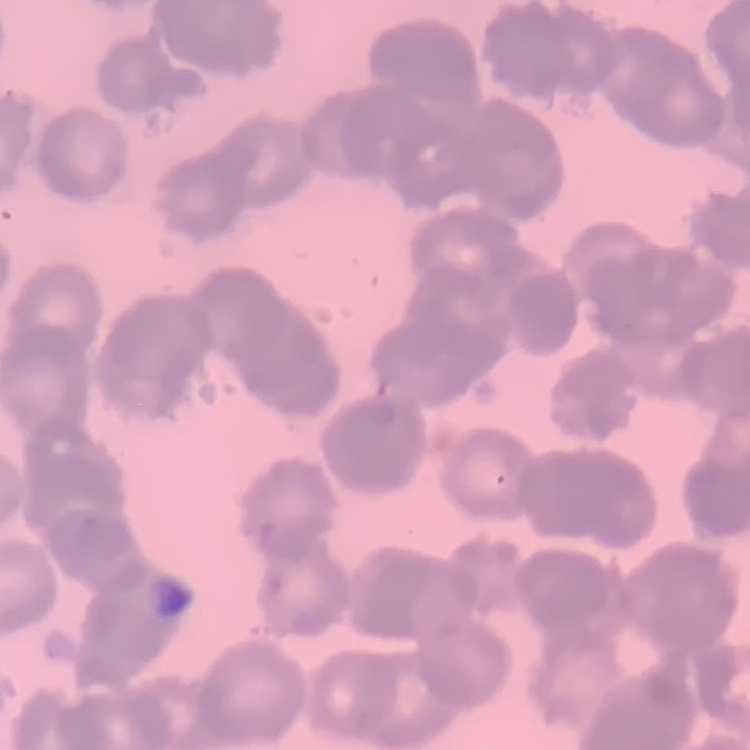

erythrocyte morphology = rouleaux formation
image type = square crop of a larger photomicrograph
stain = Field's or Giemsa
preparation = thin blood smear